Assess this cell for malaria.
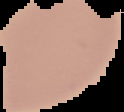
Uninfected.

Summary:
  - Preparation: thin blood film
  - Image type: cell region segmented out of the field of view; surrounding area masked to black
  - Image size: 124×112 pixels